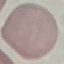
result = no malaria parasites detected
capture = smartphone through the microscope eyepiece
image type = automatically extracted cell patch, resized to 64 × 64 pixels
stain = Giemsa
preparation = thin blood smear